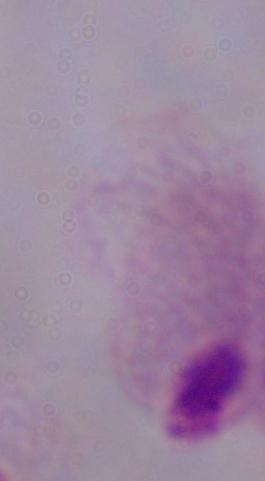
Summary:
  - Identification: trichomonad
  - Modality: micrograph
  - Magnification: 1000x